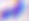
Summary:
  - Identification: Toxoplasma gondii
  - Modality: micrograph
  - Magnification: 400x